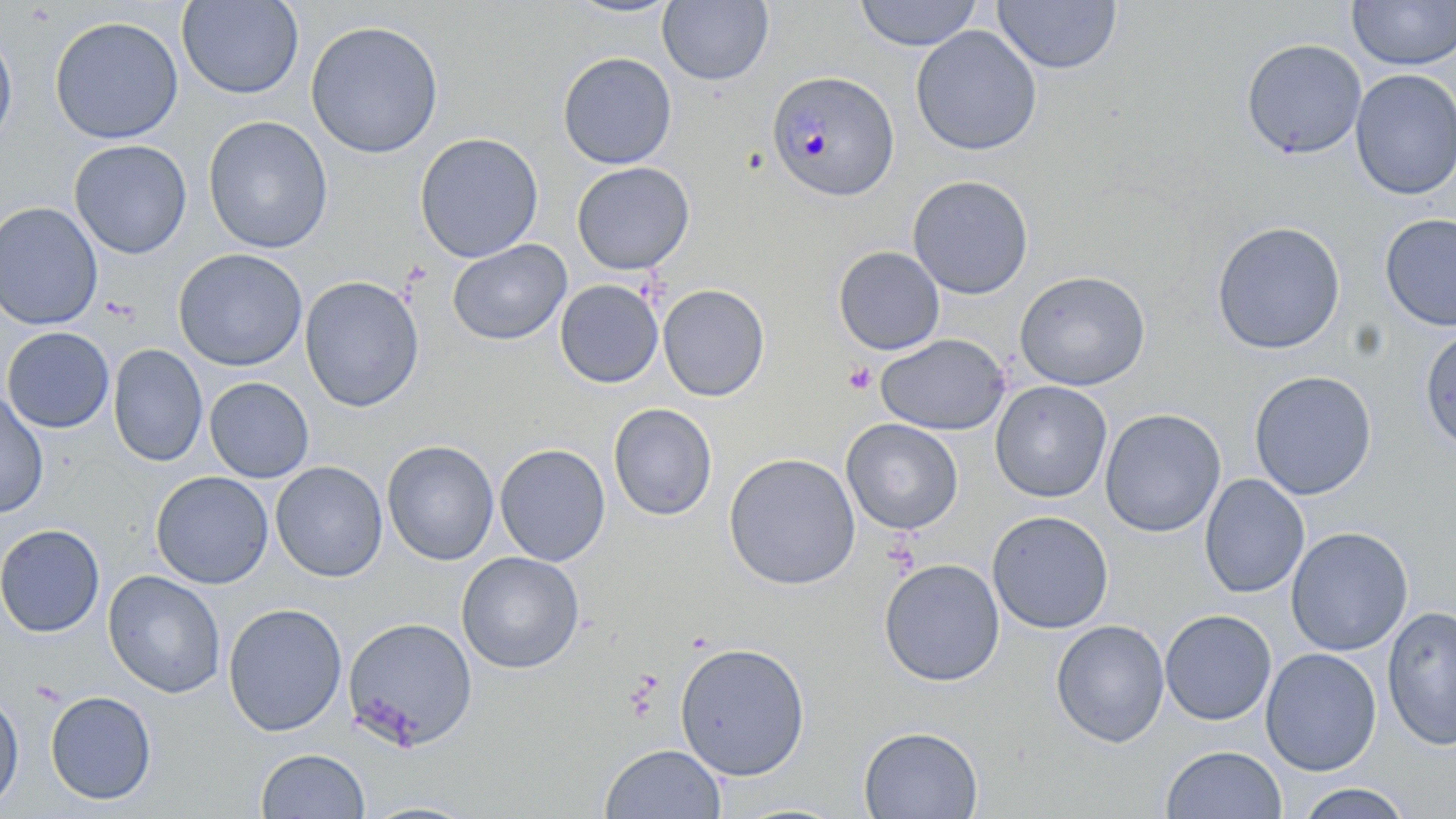

Summary:
  - Coordinate format: approximate bounding boxes as (x1, y1, x2, y2) in pixels
  - Plasmodium malariae-infected red blood cell locations: (766, 69, 899, 203)
  - Uninfected red blood cell locations: (176, 0, 304, 99), (562, 0, 683, 19), (853, 0, 983, 51), (657, 1, 774, 86), (992, 1, 1122, 75), (1347, 1, 1456, 70), (49, 15, 184, 144), (305, 19, 444, 159), (0, 25, 18, 150), (910, 25, 1042, 156), (1241, 38, 1367, 160), (557, 51, 677, 169), (1350, 68, 1456, 200), (202, 115, 334, 254), (414, 132, 544, 262), (69, 139, 192, 260), (571, 162, 695, 275), (907, 175, 1034, 299), (0, 201, 103, 330), (1378, 213, 1456, 332), (1210, 221, 1346, 355), (447, 239, 571, 346), (832, 246, 945, 355), (172, 248, 308, 372), (1014, 270, 1151, 391), (300, 275, 424, 412), (555, 279, 664, 389), (658, 283, 770, 401), (1, 327, 115, 433), (1420, 327, 1455, 454), (875, 333, 1011, 436), (107, 344, 208, 466), (1248, 370, 1378, 500), (204, 377, 314, 483), (990, 380, 1112, 503), (0, 391, 49, 518), (607, 403, 717, 521), (1100, 408, 1226, 538), (841, 418, 963, 535), (381, 440, 499, 566), (494, 443, 611, 566), (723, 452, 861, 590), (270, 461, 388, 582), (151, 471, 273, 589), (1199, 474, 1309, 598), (987, 510, 1113, 634), (0, 524, 105, 637), (1286, 526, 1413, 655), (456, 551, 585, 674), (879, 558, 1005, 687), (103, 570, 226, 699), (223, 603, 347, 736), (1381, 606, 1456, 751), (1159, 609, 1277, 725), (342, 616, 478, 751), (1050, 619, 1169, 747), (674, 641, 811, 781), (1260, 647, 1383, 776), (0, 690, 24, 812), (44, 690, 157, 805), (858, 725, 984, 819), (599, 743, 726, 819), (1160, 745, 1287, 819), (256, 748, 369, 819), (1295, 783, 1414, 818), (356, 799, 484, 819)
  - Platelet locations: (843, 362, 876, 394)
  - Slide-level diagnosis: Plasmodium malariae
  - Magnification: 1000x
  - Field of view: one of a larger specimen
  - Modality: optical microscopy
  - Preparation: thin blood film
  - Stain: May-Grünwald-Giemsa
  - Image size: 1456×819 pixels